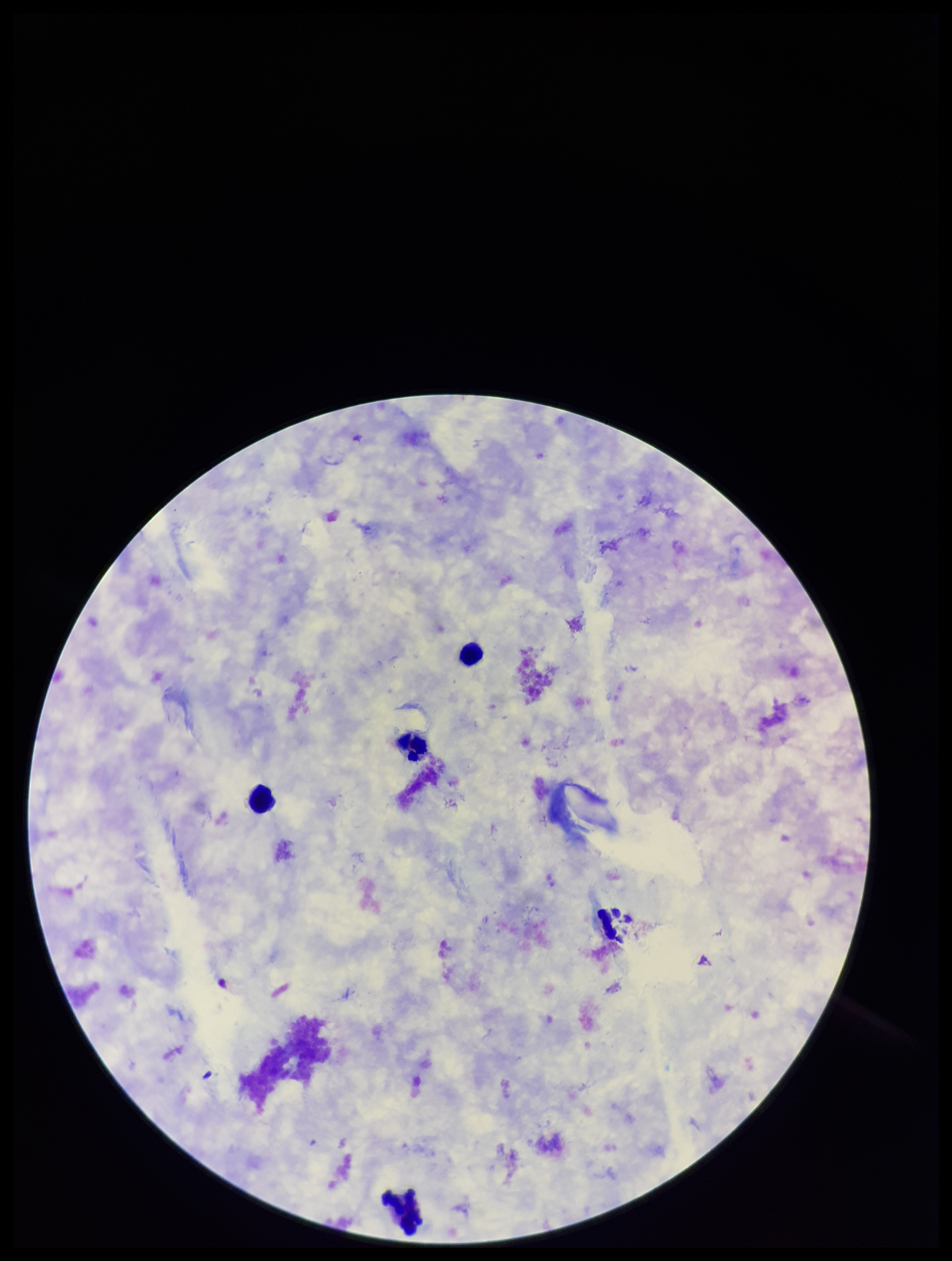
Summary:
  - Patient malaria status: negative
  - Leukocyte count: 3
  - Preparation: thick smear
  - Field of view: single
  - Stain: Giemsa
  - Capture: smartphone photograph through the microscope eyepiece
  - Image size: 952×1261 pixels
  - Plasmodium parasites: none detected
  - Parasite count: 0